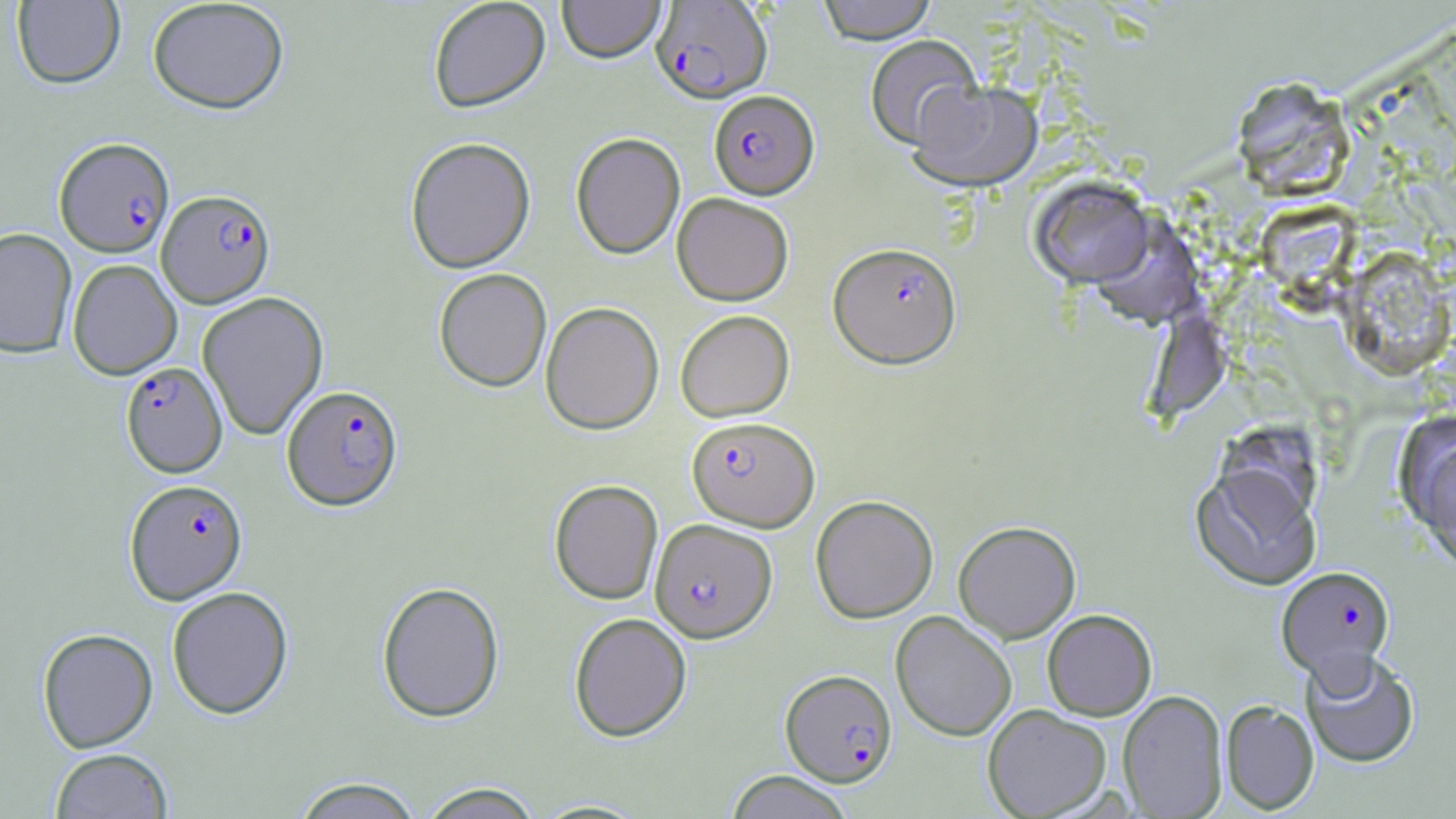
Summary:
  - Coordinate format: approximate bounding boxes as (x1,y1)-(x2,y2) corner pairs in pixels
  - Uninfected red blood cell locations: (11,0)-(125,89), (428,0)-(551,114), (557,0)-(666,64), (816,0)-(939,45), (146,1)-(289,115), (864,35)-(984,150), (1231,77)-(1356,201), (908,80)-(1042,192), (570,132)-(685,261), (404,137)-(537,274), (1029,177)-(1154,288), (672,193)-(794,306), (1256,201)-(1358,303), (1090,212)-(1205,329), (0,228)-(77,358), (1341,248)-(1455,380), (67,259)-(182,379), (434,268)-(552,392), (197,292)-(329,440), (540,302)-(664,435), (675,310)-(794,422), (1146,310)-(1231,420), (1401,418)-(1456,568), (1191,464)-(1321,591), (549,479)-(663,605), (810,495)-(938,623), (953,521)-(1081,643), (376,581)-(505,723), (166,586)-(294,719), (1042,609)-(1157,721), (891,611)-(1017,741), (569,613)-(692,742), (37,628)-(158,752), (1300,648)-(1421,768), (1117,690)-(1228,818), (1220,700)-(1319,814), (982,704)-(1112,818), (49,749)-(173,819), (724,771)-(855,819), (289,777)-(424,818), (416,783)-(545,818), (529,799)-(653,818)
  - Plasmodium falciparum-infected red blood cell locations: (650,1)-(773,105), (708,90)-(819,200), (54,137)-(175,257), (157,189)-(275,308), (827,242)-(962,369), (120,362)-(227,477), (281,385)-(403,512), (687,417)-(819,531), (125,478)-(248,604), (650,519)-(777,643), (1277,565)-(1395,681), (780,669)-(897,787)
  - Slide-level diagnosis: Plasmodium falciparum
  - Field of view: one of a larger specimen
  - Stain: May-Grünwald-Giemsa
  - Image size: 1456×819 pixels
  - Preparation: thin blood smear
  - Magnification: 1000x
  - Modality: light microscopy